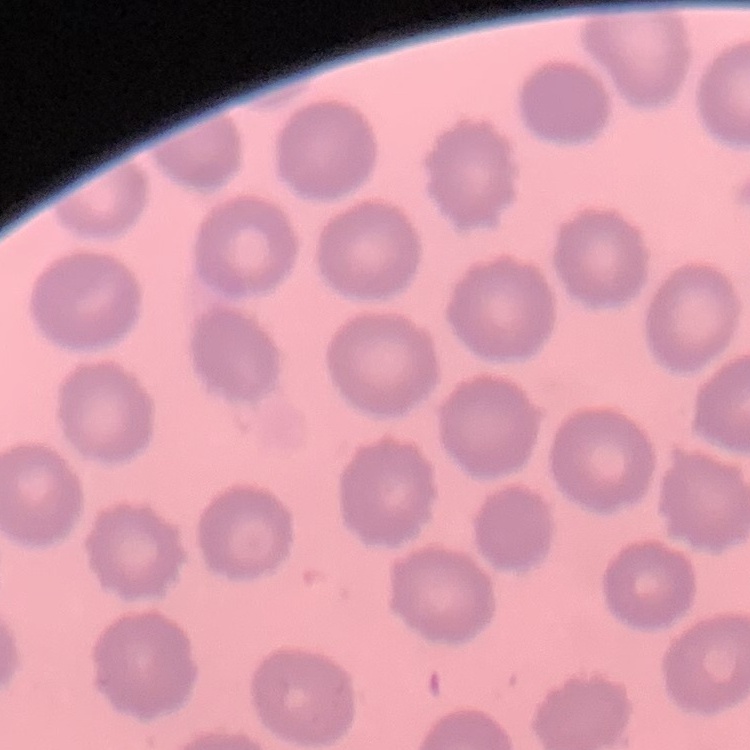

Summary:
  - Red blood cell morphology: no rouleaux formation
  - Preparation: thin peripheral smear
  - Image type: square crop of a larger photomicrograph
  - Stain: Field's or Giemsa